Identify the blood parasite species.
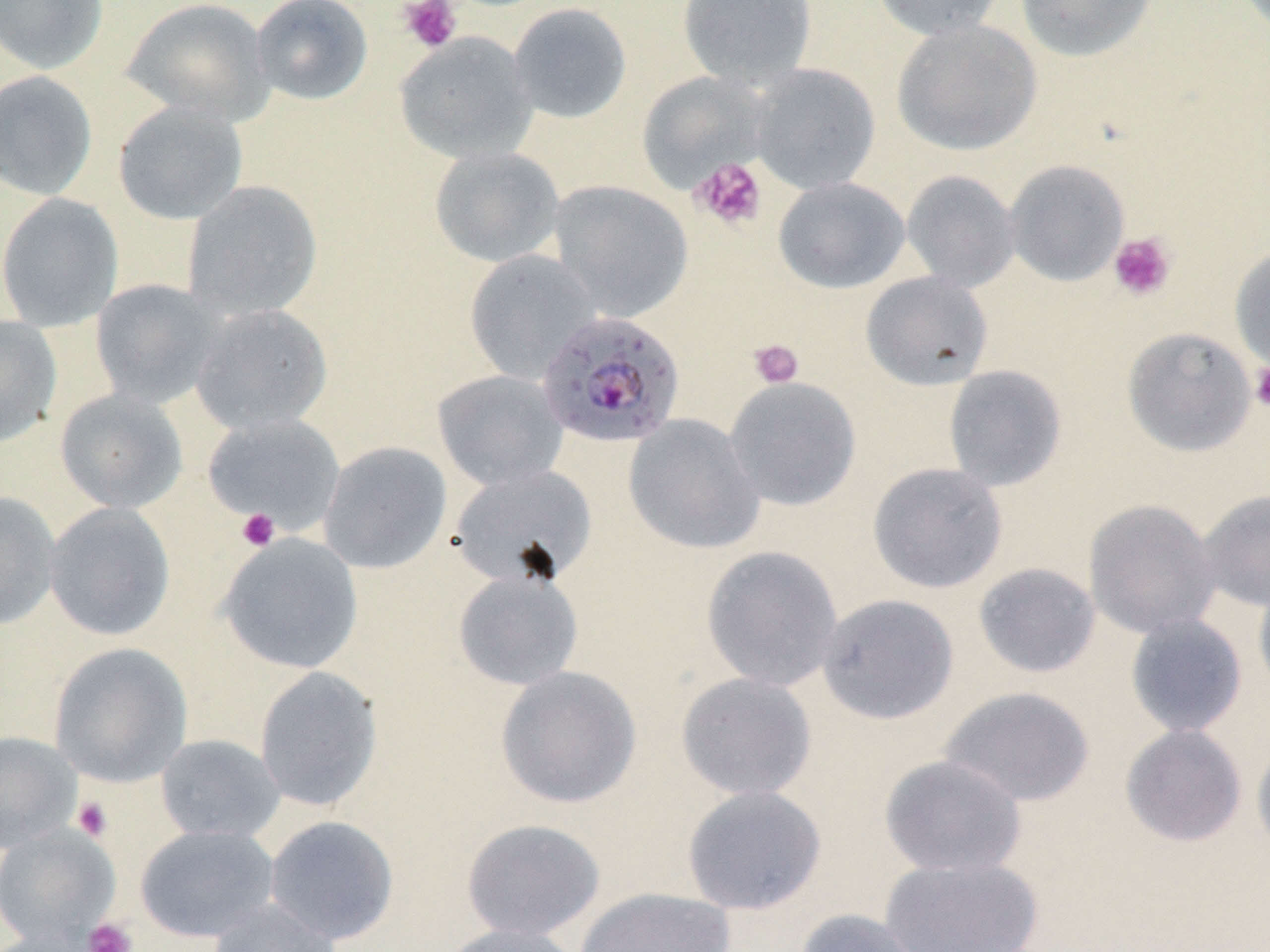
Plasmodium falciparum.

Summary:
  - Coordinate format: approximate bounding boxes as (x1, y1, x2, y2) in pixels
  - Uninfected red blood cell locations: (0, 0, 109, 75), (122, 0, 275, 126), (250, 0, 374, 106), (677, 0, 817, 86), (870, 0, 1009, 40), (1015, 0, 1157, 62), (508, 2, 632, 123), (892, 19, 1042, 156), (394, 32, 538, 166), (749, 64, 880, 195), (0, 70, 98, 201), (637, 71, 771, 192), (113, 100, 248, 225), (429, 146, 564, 268), (1004, 159, 1129, 286), (902, 170, 1020, 292), (773, 176, 910, 294), (182, 180, 323, 321), (550, 180, 692, 322), (0, 193, 123, 331), (1230, 246, 1270, 374), (464, 249, 599, 383), (861, 271, 994, 390), (90, 279, 223, 409), (191, 303, 332, 435), (0, 315, 62, 445), (1122, 326, 1257, 457), (943, 365, 1067, 491), (432, 369, 569, 492), (724, 376, 861, 511), (55, 388, 188, 513), (202, 413, 346, 534), (623, 414, 765, 555), (318, 441, 452, 574), (867, 462, 1008, 594), (449, 463, 598, 589), (1197, 488, 1270, 613), (0, 491, 61, 630), (1083, 498, 1221, 640), (44, 502, 176, 641), (217, 533, 363, 674), (701, 546, 844, 692), (973, 562, 1101, 678), (453, 569, 583, 691), (1253, 574, 1270, 702), (817, 593, 959, 725), (1125, 613, 1247, 738), (49, 642, 193, 786), (495, 665, 642, 809), (254, 666, 383, 812), (675, 672, 818, 801), (940, 686, 1095, 808), (1120, 724, 1247, 847), (0, 731, 80, 850), (155, 734, 285, 843), (1251, 735, 1270, 861), (879, 754, 1027, 878), (682, 785, 827, 915), (264, 815, 400, 945), (461, 818, 606, 941), (0, 825, 119, 945), (135, 825, 279, 942), (879, 856, 1044, 952), (575, 887, 736, 952), (208, 896, 341, 952), (793, 908, 928, 952), (439, 922, 585, 952)
  - Platelet locations: (398, 0, 462, 53), (691, 158, 768, 231), (1108, 232, 1176, 301), (748, 339, 804, 388), (1250, 364, 1270, 412), (236, 507, 280, 552), (73, 797, 113, 841), (83, 917, 137, 952)
  - Plasmodium falciparum-infected red blood cell locations: (535, 310, 685, 448)
  - Field of view: single
  - Image size: 1270×952 pixels
  - Stain: May-Grünwald-Giemsa
  - Preparation: thin blood smear
  - Modality: optical microscopy
  - Magnification: 1000x